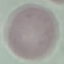
malaria status = uninfected
image type = automatically extracted cell patch, resized to 64 × 64 pixels
preparation = thin blood film
stain = Giemsa
capture = smartphone camera at the microscope eyepiece